State the blood parasite species.
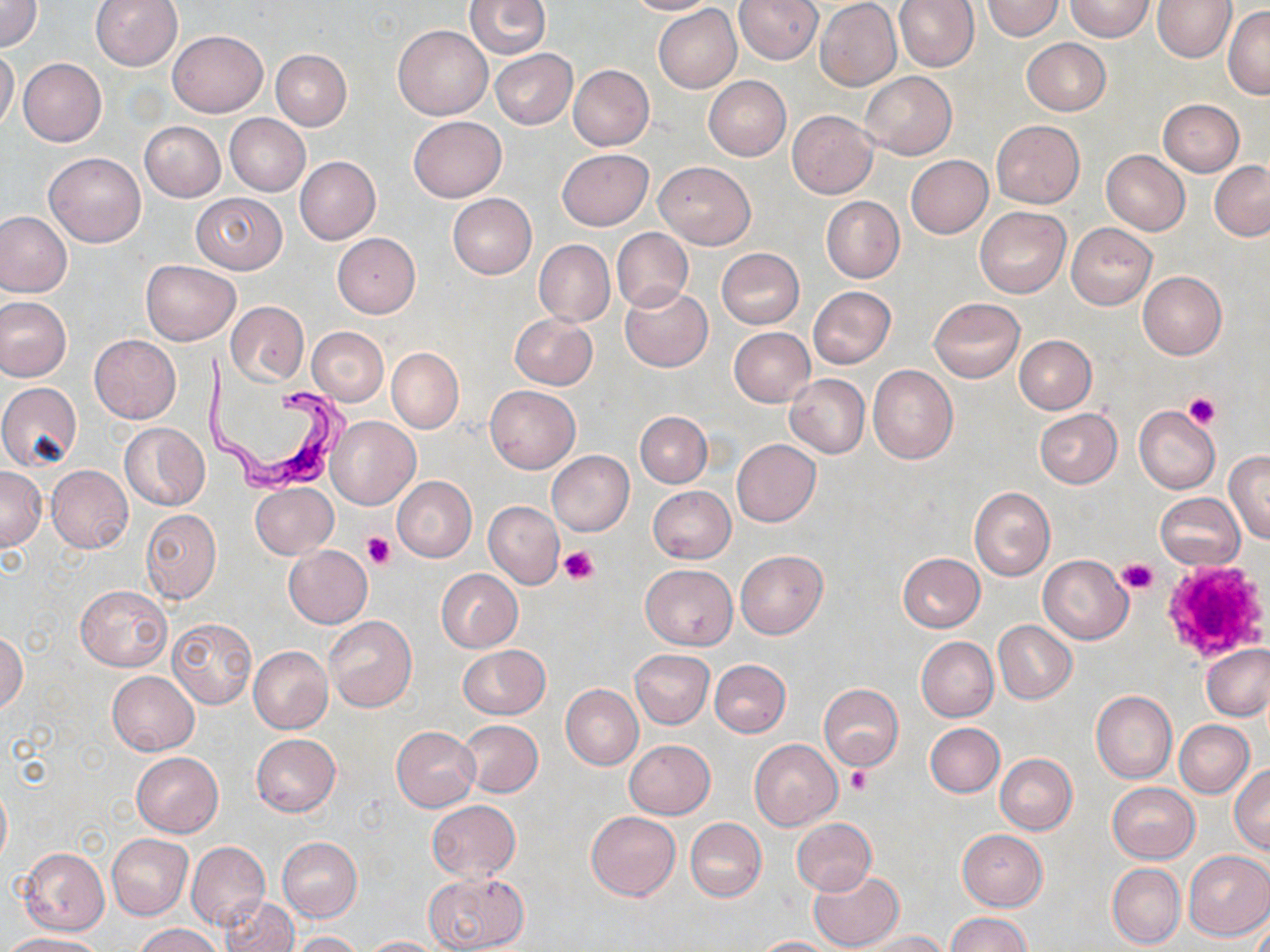

Trypanosoma brucei.

magnification = 1000x
uninfected red blood cell locations = approximate bounding boxes as named x1/y1/x2/y2 corners in pixels: (x1=0, y1=0, x2=42, y2=51), (x1=89, y1=0, x2=183, y2=70), (x1=465, y1=0, x2=551, y2=59), (x1=625, y1=0, x2=719, y2=16), (x1=735, y1=0, x2=822, y2=64), (x1=895, y1=0, x2=979, y2=72), (x1=982, y1=0, x2=1063, y2=40), (x1=1154, y1=0, x2=1237, y2=62), (x1=1065, y1=1, x2=1153, y2=41), (x1=815, y1=2, x2=901, y2=89), (x1=1223, y1=5, x2=1270, y2=98), (x1=654, y1=6, x2=741, y2=91), (x1=393, y1=24, x2=492, y2=120), (x1=167, y1=29, x2=268, y2=118), (x1=1022, y1=38, x2=1110, y2=115), (x1=0, y1=48, x2=19, y2=133), (x1=271, y1=49, x2=352, y2=129), (x1=490, y1=49, x2=578, y2=129), (x1=18, y1=58, x2=107, y2=146), (x1=568, y1=65, x2=654, y2=150), (x1=859, y1=71, x2=956, y2=159), (x1=703, y1=76, x2=791, y2=160), (x1=1158, y1=99, x2=1244, y2=175), (x1=787, y1=111, x2=877, y2=199), (x1=224, y1=114, x2=309, y2=196), (x1=409, y1=116, x2=506, y2=201), (x1=992, y1=120, x2=1084, y2=208), (x1=139, y1=121, x2=225, y2=202), (x1=558, y1=148, x2=653, y2=229), (x1=1101, y1=150, x2=1189, y2=236), (x1=44, y1=152, x2=145, y2=247), (x1=906, y1=155, x2=993, y2=239), (x1=295, y1=156, x2=381, y2=245), (x1=654, y1=161, x2=755, y2=249), (x1=1209, y1=161, x2=1270, y2=241), (x1=190, y1=193, x2=287, y2=274), (x1=448, y1=193, x2=537, y2=278), (x1=821, y1=196, x2=904, y2=283), (x1=974, y1=207, x2=1070, y2=297), (x1=0, y1=211, x2=72, y2=297), (x1=1067, y1=223, x2=1156, y2=309), (x1=612, y1=228, x2=693, y2=311), (x1=333, y1=233, x2=420, y2=317), (x1=534, y1=240, x2=615, y2=326), (x1=716, y1=247, x2=806, y2=330), (x1=141, y1=260, x2=239, y2=345), (x1=1136, y1=271, x2=1226, y2=360), (x1=621, y1=285, x2=712, y2=372), (x1=808, y1=286, x2=896, y2=368), (x1=0, y1=297, x2=71, y2=381), (x1=930, y1=297, x2=1025, y2=382), (x1=226, y1=302, x2=307, y2=385), (x1=510, y1=313, x2=597, y2=389), (x1=307, y1=327, x2=388, y2=405), (x1=729, y1=327, x2=815, y2=407), (x1=89, y1=334, x2=181, y2=423), (x1=1013, y1=335, x2=1096, y2=414), (x1=386, y1=347, x2=464, y2=433), (x1=868, y1=365, x2=959, y2=465), (x1=784, y1=373, x2=869, y2=458), (x1=0, y1=382, x2=82, y2=470), (x1=486, y1=386, x2=579, y2=472), (x1=1134, y1=405, x2=1221, y2=493), (x1=1034, y1=409, x2=1122, y2=488), (x1=635, y1=410, x2=711, y2=487), (x1=642, y1=412, x2=720, y2=562), (x1=326, y1=416, x2=420, y2=510), (x1=119, y1=423, x2=207, y2=510), (x1=732, y1=439, x2=820, y2=526), (x1=547, y1=450, x2=634, y2=535), (x1=1225, y1=451, x2=1270, y2=542), (x1=46, y1=465, x2=134, y2=553), (x1=0, y1=467, x2=45, y2=550), (x1=392, y1=476, x2=477, y2=562), (x1=250, y1=482, x2=337, y2=559), (x1=648, y1=485, x2=736, y2=563), (x1=969, y1=487, x2=1055, y2=580), (x1=1155, y1=492, x2=1245, y2=570), (x1=483, y1=501, x2=563, y2=589), (x1=141, y1=509, x2=221, y2=604), (x1=283, y1=545, x2=373, y2=628), (x1=736, y1=550, x2=828, y2=639), (x1=897, y1=552, x2=985, y2=632), (x1=1038, y1=555, x2=1133, y2=643), (x1=640, y1=564, x2=737, y2=648), (x1=436, y1=568, x2=523, y2=652), (x1=75, y1=585, x2=172, y2=671), (x1=323, y1=615, x2=417, y2=712), (x1=166, y1=616, x2=257, y2=710), (x1=993, y1=620, x2=1077, y2=703), (x1=0, y1=633, x2=26, y2=712), (x1=916, y1=636, x2=998, y2=721), (x1=458, y1=644, x2=550, y2=719), (x1=1202, y1=645, x2=1269, y2=720), (x1=249, y1=646, x2=333, y2=732), (x1=630, y1=649, x2=714, y2=729), (x1=710, y1=659, x2=791, y2=736), (x1=108, y1=670, x2=200, y2=755), (x1=560, y1=684, x2=642, y2=770), (x1=819, y1=684, x2=904, y2=770), (x1=1090, y1=689, x2=1177, y2=783), (x1=1174, y1=719, x2=1254, y2=797), (x1=457, y1=720, x2=543, y2=797), (x1=925, y1=722, x2=1004, y2=797), (x1=391, y1=726, x2=480, y2=810), (x1=251, y1=734, x2=340, y2=817), (x1=750, y1=738, x2=843, y2=831), (x1=625, y1=740, x2=715, y2=819), (x1=132, y1=752, x2=223, y2=836), (x1=995, y1=753, x2=1077, y2=835), (x1=1230, y1=765, x2=1270, y2=855), (x1=0, y1=780, x2=11, y2=867), (x1=1107, y1=782, x2=1199, y2=863), (x1=427, y1=800, x2=519, y2=881), (x1=585, y1=811, x2=680, y2=900), (x1=790, y1=817, x2=877, y2=895), (x1=686, y1=819, x2=766, y2=900), (x1=958, y1=830, x2=1047, y2=910), (x1=107, y1=834, x2=193, y2=920), (x1=278, y1=837, x2=362, y2=920), (x1=186, y1=841, x2=269, y2=930), (x1=18, y1=847, x2=109, y2=936), (x1=1182, y1=849, x2=1270, y2=941), (x1=1107, y1=864, x2=1185, y2=949), (x1=807, y1=869, x2=903, y2=951), (x1=423, y1=872, x2=528, y2=951), (x1=219, y1=896, x2=298, y2=952), (x1=1252, y1=910, x2=1269, y2=952), (x1=947, y1=912, x2=1030, y2=952), (x1=133, y1=924, x2=222, y2=952), (x1=862, y1=930, x2=949, y2=951), (x1=293, y1=931, x2=362, y2=952), (x1=4, y1=934, x2=105, y2=952), (x1=359, y1=936, x2=444, y2=952), (x1=749, y1=936, x2=839, y2=952)
field of view = single
image size = 1270×952 pixels
preparation = thin blood smear
stain = May-Grünwald-Giemsa
Trypanosoma brucei locations = approximate bounding boxes as named x1/y1/x2/y2 corners in pixels: (x1=207, y1=354, x2=343, y2=491)
modality = light microscopy
platelet locations = approximate bounding boxes as named x1/y1/x2/y2 corners in pixels: (x1=1183, y1=389, x2=1221, y2=427), (x1=361, y1=533, x2=395, y2=569), (x1=556, y1=546, x2=599, y2=583), (x1=1118, y1=557, x2=1158, y2=595), (x1=1164, y1=560, x2=1267, y2=663), (x1=845, y1=767, x2=872, y2=795)